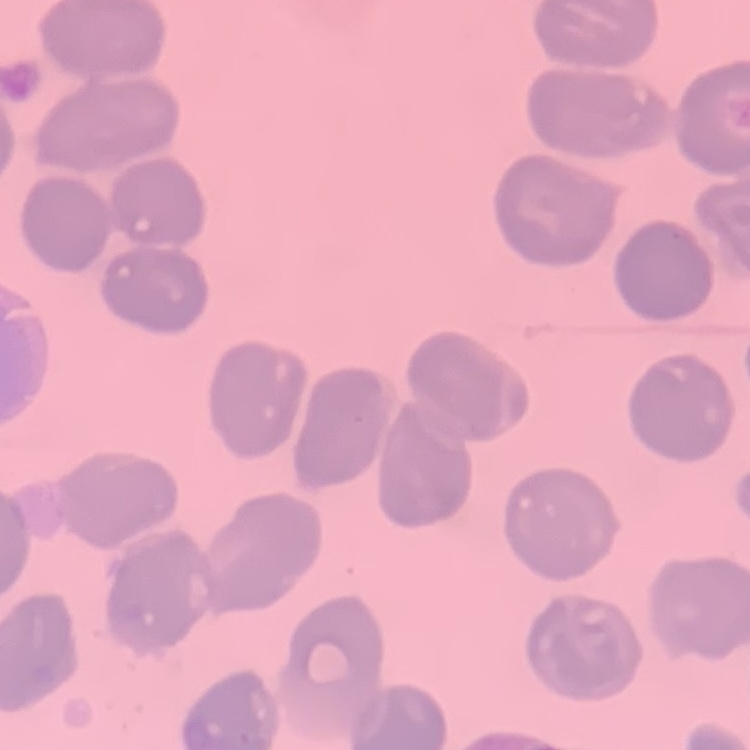

red_blood_cell_morphology: no rouleaux formation
image_type: square crop of a larger photomicrograph
preparation: thin peripheral smear
stain: Field's or Giemsa